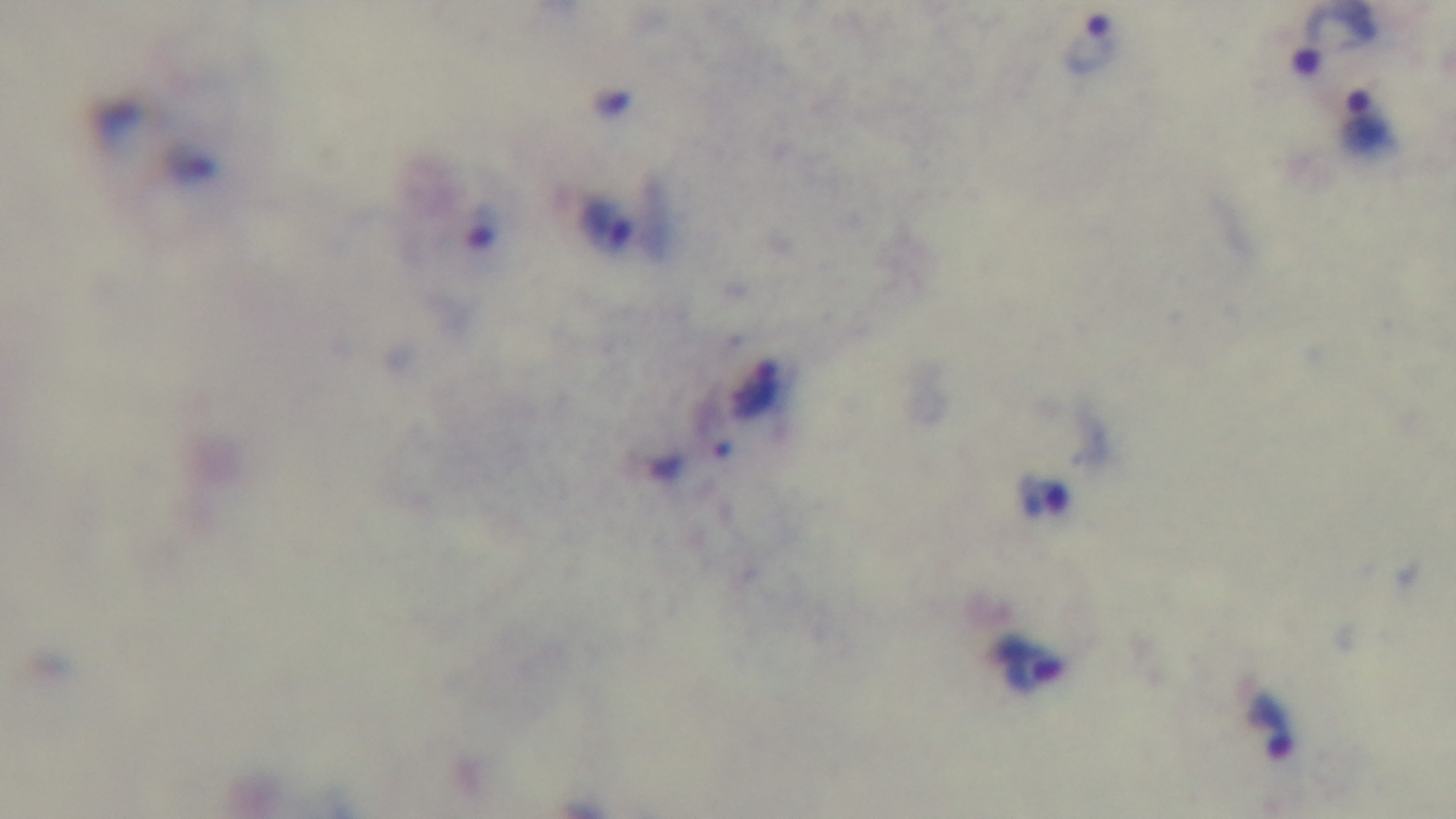
objective: 100x oil immersion
capture: mounted 4K digital camera
stain: Giemsa
malaria_status: infected
modality: light microscopy
field_of_view: one from the slide
preparation: thick blood film